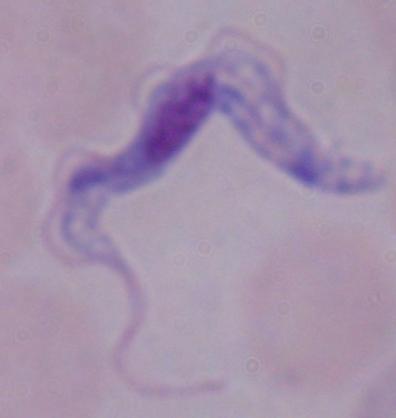

Summary:
  - Identification: trypanosome
  - Magnification: 1000x
  - Modality: photomicrograph